Describe the morphology of the erythrocytes.
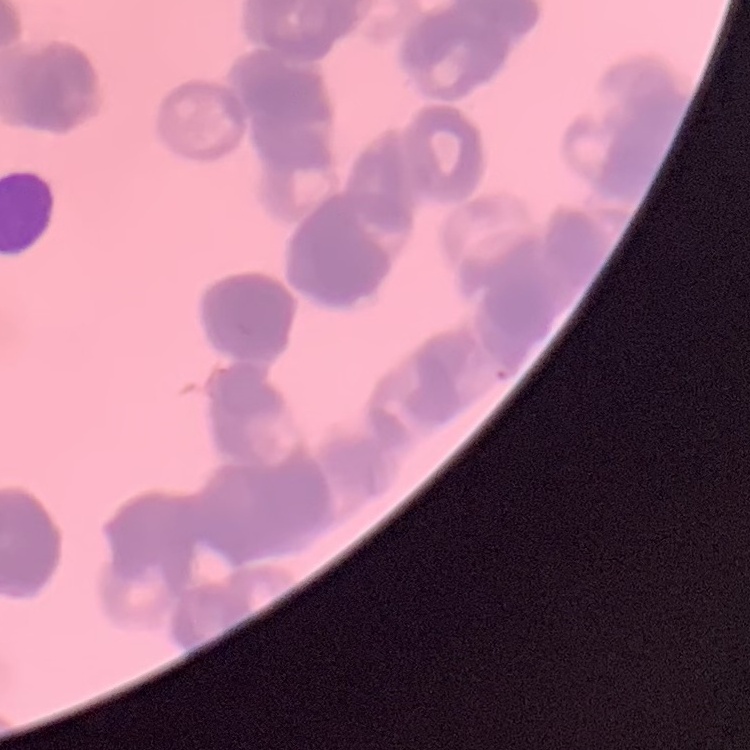
They show rouleaux formation.

Field's or Giemsa stain. Thin blood smear. Square crop of a larger photomicrograph.